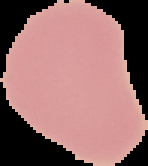

image size = 148×166 pixels
result = no Plasmodium parasites seen
preparation = thin blood film
image type = segmented cell region on a black background